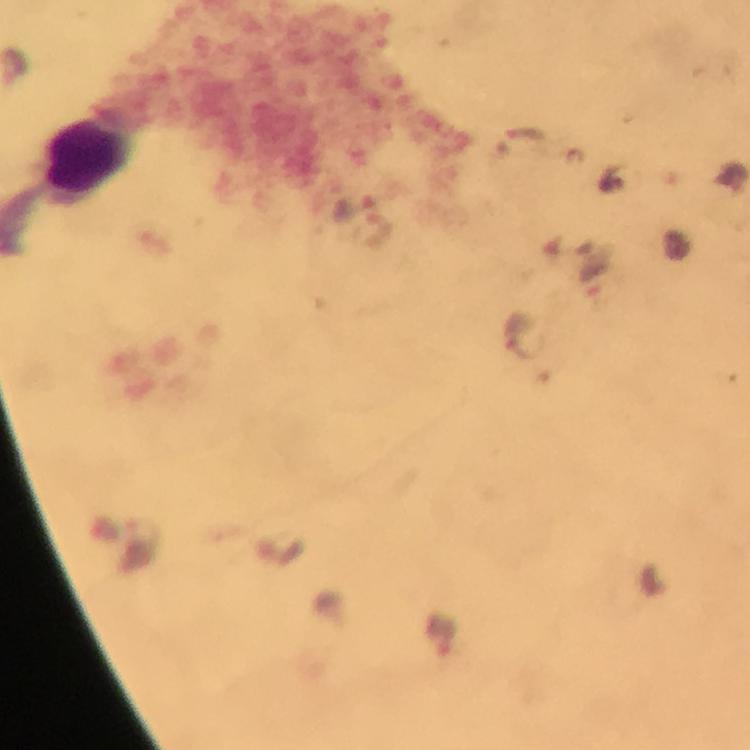 Approximate centers as {x, y} in pixels. Malaria parasite locations: {594, 272}, {522, 335}, {441, 637}. Leukocyte locations: {90, 156}. Giemsa-stained preparation. Cropped region of a single field of view. Photographed through the microscope with a smartphone camera. Image is 750×750 pixels. Thick smear. Immersion oil was used. From a malaria diagnostic workup. 100x magnification.